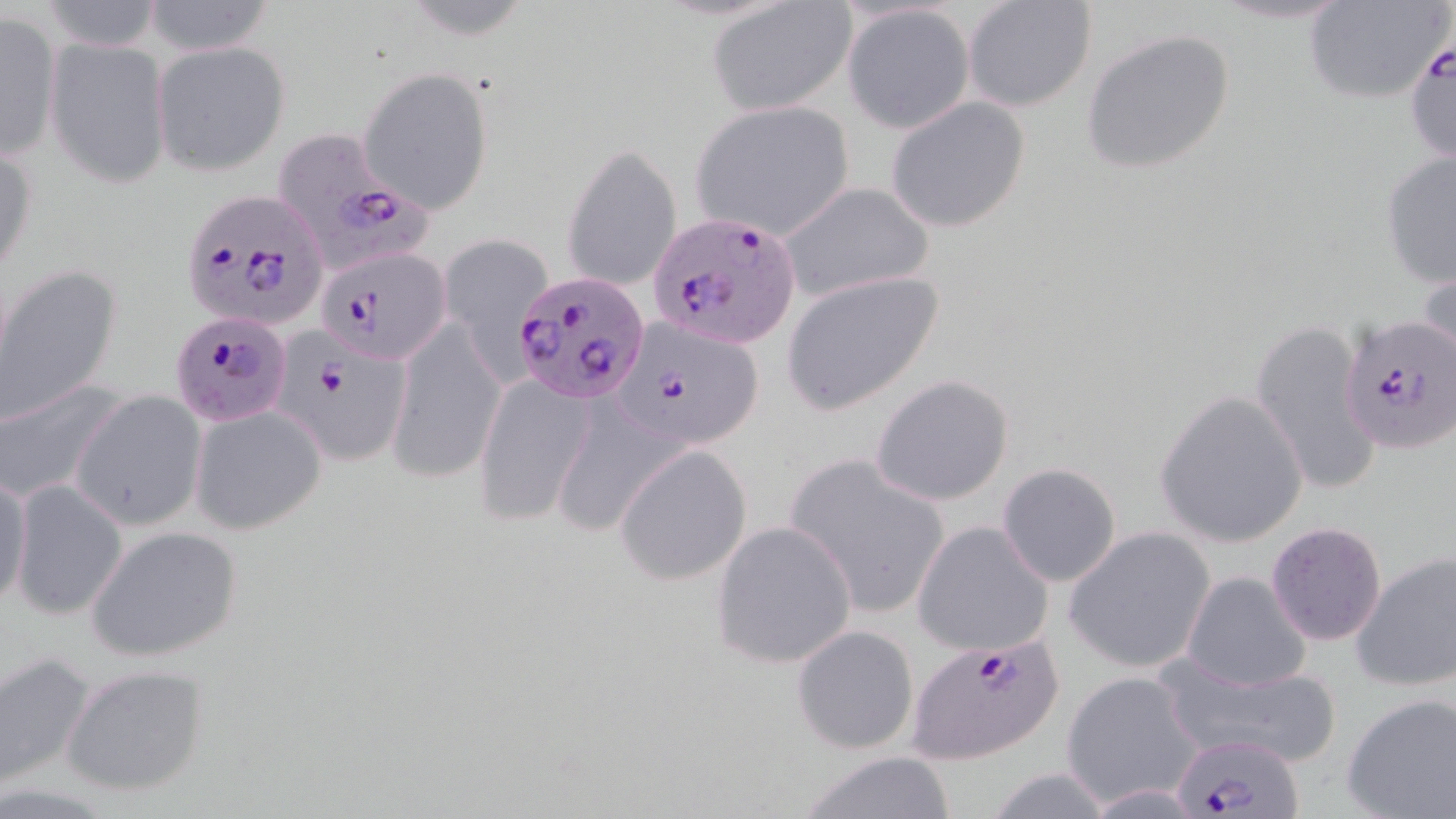

Summary:
  - Coordinate format: approximate bounding boxes as (x1,y1)-(x2,y2) corner pairs in pixels
  - Plasmodium falciparum-infected red blood cell locations: (1405,30)-(1455,164), (270,126)-(427,265), (179,187)-(329,332), (651,212)-(799,347), (317,246)-(450,364), (513,267)-(650,402), (1339,312)-(1455,453), (169,314)-(293,426), (609,317)-(764,448), (274,337)-(413,465), (907,630)-(1065,764), (1169,733)-(1305,819)
  - Uninfected red blood cell locations: (141,0)-(279,57), (1204,0)-(1360,26), (1301,0)-(1453,106), (38,1)-(165,51), (962,1)-(1097,114), (708,2)-(856,117), (841,3)-(974,133), (0,12)-(62,163), (1081,28)-(1236,176), (48,36)-(172,187), (151,40)-(291,176), (359,67)-(495,213), (885,97)-(1031,233), (689,100)-(857,243), (1,137)-(37,282), (562,139)-(683,293), (1380,152)-(1456,288), (776,182)-(935,302), (435,232)-(549,366), (1418,253)-(1456,376), (1,266)-(121,428), (782,270)-(944,415), (387,317)-(506,482), (1250,317)-(1382,496), (475,374)-(595,525), (870,374)-(1014,507), (0,380)-(121,505), (1153,390)-(1309,548), (69,391)-(206,531), (189,402)-(326,534), (615,444)-(753,586), (784,456)-(953,620), (996,462)-(1123,587), (0,468)-(31,616), (10,478)-(127,620), (711,521)-(858,670), (912,521)-(1053,656), (1265,521)-(1387,646), (84,525)-(245,664), (1062,527)-(1216,675), (1351,550)-(1456,693), (1181,570)-(1314,692), (792,624)-(919,755), (0,653)-(95,791), (1162,657)-(1338,770), (61,664)-(210,797), (1059,671)-(1203,808), (1342,692)-(1456,819), (795,751)-(960,819)
  - Slide-level diagnosis: Plasmodium falciparum
  - Preparation: thin blood film
  - Field of view: single
  - Image size: 1456×819 pixels
  - Modality: optical microscopy
  - Magnification: 1000x
  - Stain: May-Grünwald-Giemsa